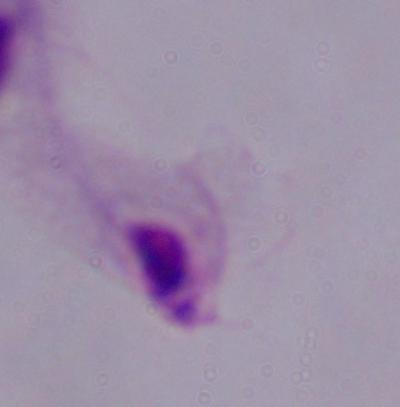

identification = trichomonad
modality = photomicrograph
magnification = 1000x